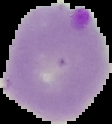
Summary:
  - Malaria status: parasitized
  - Preparation: thin blood film
  - Image size: 112×124 pixels
  - Image type: segmented cell region with the area outside set to black